Report the malaria status of this cell.
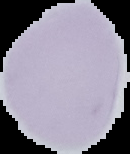

It is uninfected.

Summary:
  - Preparation: thin blood smear
  - Image type: segmented cell region with the area outside set to black
  - Image size: 130×154 pixels